Locate every leukocyte (white blood cell).
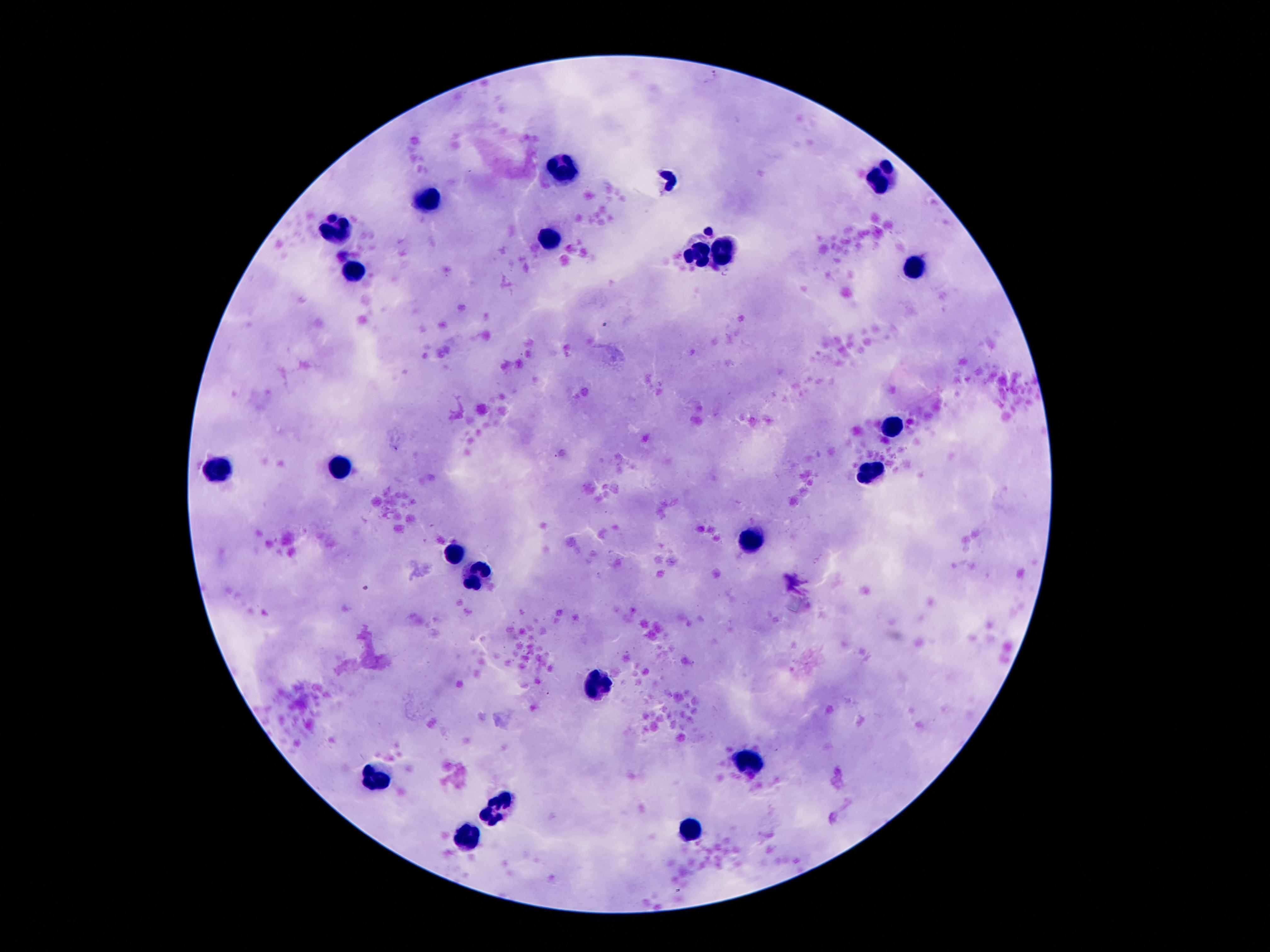

Approximate centers as {x, y} in pixels.
Leukocytes: {569, 170}, {885, 176}, {432, 201}, {340, 226}, {549, 234}, {697, 254}, {727, 254}, {353, 267}, {911, 267}, {890, 428}, {343, 467}, {218, 470}, {867, 473}, {748, 539}, {455, 552}, {478, 579}, {600, 685}, {753, 756}, {376, 776}, {506, 802}, {489, 820}, {692, 827}, {470, 835}.

Image is 1270×952 pixels. Smartphone photograph taken through the microscope eyepiece. 100x magnification. Patient malaria status: negative. Thick peripheral-blood smear. Giemsa stain. One field from this slide.